State which parasite is depicted.
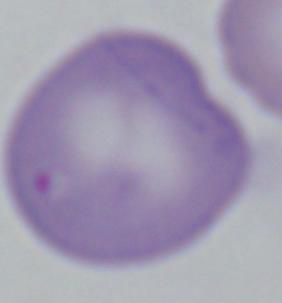
This is Babesia.

modality: micrograph
magnification: 1000x